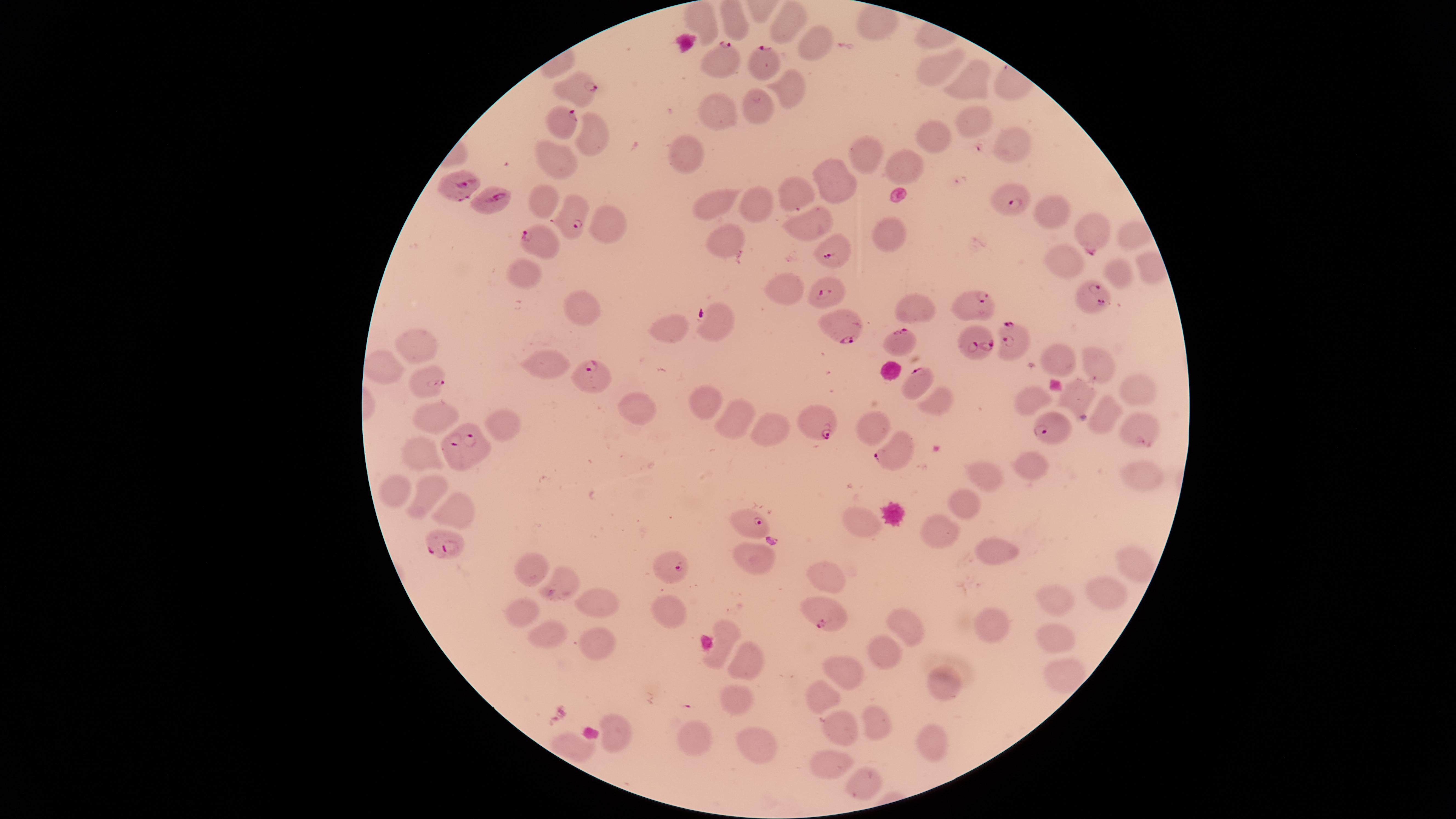
Approximate marker points as {x, y} in pixels. Uninfected red blood cells: {731, 17}, {703, 19}, {792, 21}, {818, 39}, {946, 58}, {976, 81}, {785, 94}, {715, 106}, {762, 108}, {974, 123}, {931, 132}, {595, 134}, {1004, 147}, {687, 152}, {857, 158}, {547, 162}, {906, 165}, {837, 180}, {793, 195}, {544, 198}, {711, 202}, {758, 202}, {1053, 208}, {807, 224}, {607, 226}, {892, 231}, {721, 249}, {1064, 256}, {1120, 270}, {523, 271}, {784, 287}, {578, 306}, {913, 307}, {671, 328}, {427, 341}, {1052, 360}, {1098, 364}, {551, 368}, {382, 369}, {1136, 391}, {703, 394}, {1028, 394}, {1075, 398}, {938, 401}, {436, 408}, {640, 410}, {1100, 412}, {738, 418}, {1136, 421}, {498, 425}, {776, 425}, {870, 426}, {419, 450}, {1027, 465}, {983, 475}, {1137, 477}, {394, 484}, {431, 492}, {967, 503}, {450, 509}, {857, 519}, {940, 524}, {995, 555}, {759, 556}, {1129, 563}, {532, 570}, {823, 580}, {557, 583}, {1103, 593}, {1054, 597}, {592, 604}, {665, 615}, {523, 616}, {988, 623}, {907, 625}, {724, 631}, {547, 632}, {1052, 636}, {592, 640}, {884, 652}, {740, 665}, {1060, 665}, {842, 666}, {945, 682}, {821, 692}, {739, 699}, {871, 716}, {835, 729}, {620, 735}, {694, 736}, {756, 741}, {930, 744}, {839, 758}, {865, 778}. Parasitized red blood cells: {720, 54}, {770, 61}, {579, 88}, {561, 118}, {465, 187}, {487, 201}, {1013, 203}, {574, 218}, {1092, 234}, {543, 242}, {833, 252}, {827, 288}, {1090, 298}, {972, 302}, {716, 323}, {841, 327}, {900, 343}, {978, 344}, {1014, 344}, {590, 378}, {428, 379}, {918, 381}, {819, 423}, {1049, 430}, {468, 451}, {893, 454}, {755, 521}, {440, 543}, {671, 567}, {821, 617}. Giemsa-stained preparation. Image is 1456×819 pixels. Thin blood smear. One field of view of the specimen. Species: Plasmodium falciparum. Smartphone photograph through the microscope eyepiece. Circular visible region. Presence: malaria parasites identified.